State the preparation type.
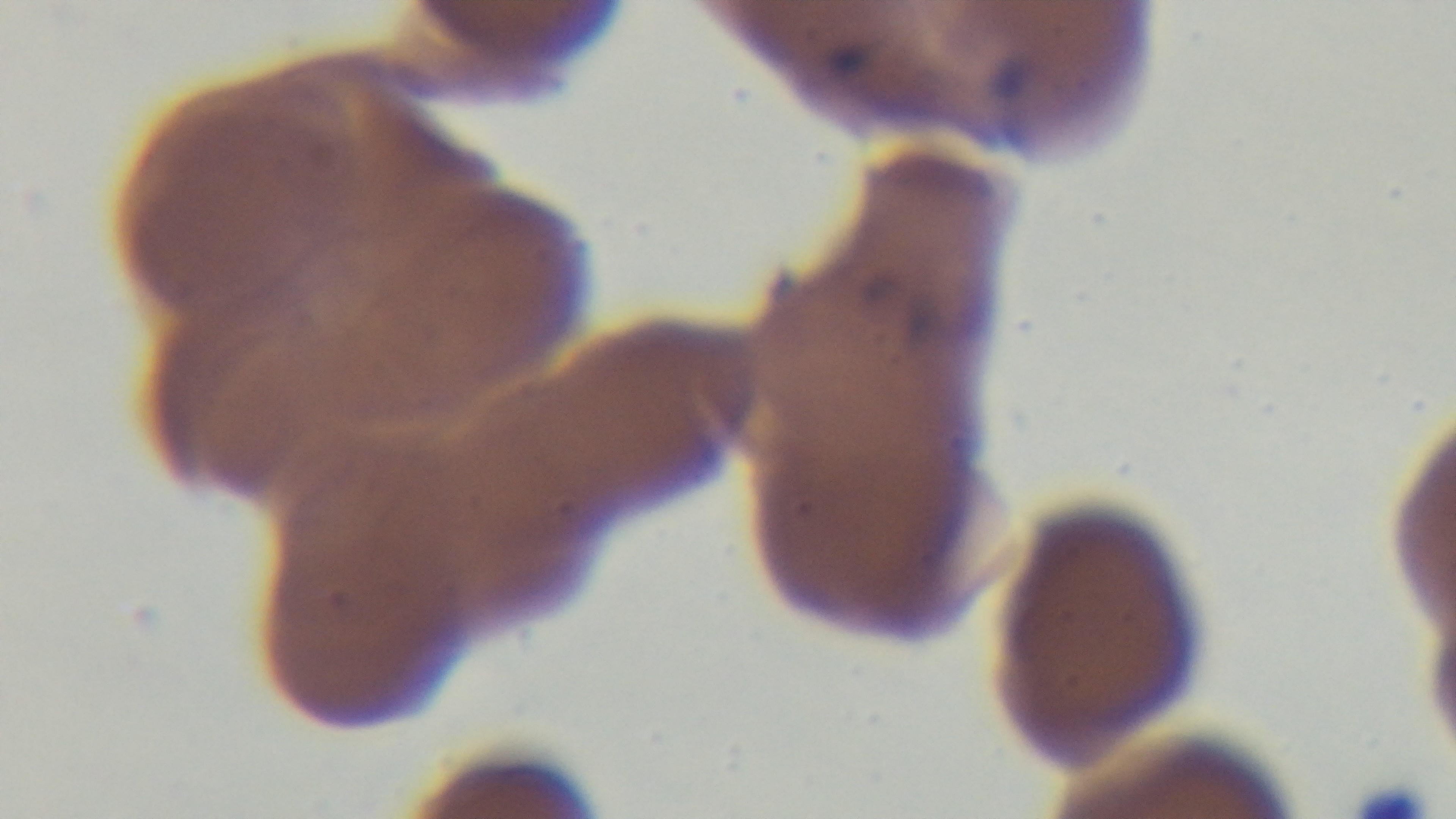
It is a thin blood film.

Summary:
  - Capture: mounted 4K digital camera
  - Modality: light microscopy
  - Stain: Giemsa
  - Objective: 100x oil immersion
  - Malaria status: positive
  - Field of view: single